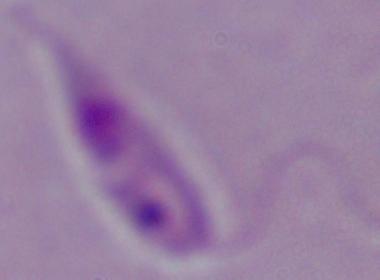 A Leishmania parasite is shown. Micrograph. 1000x magnification.